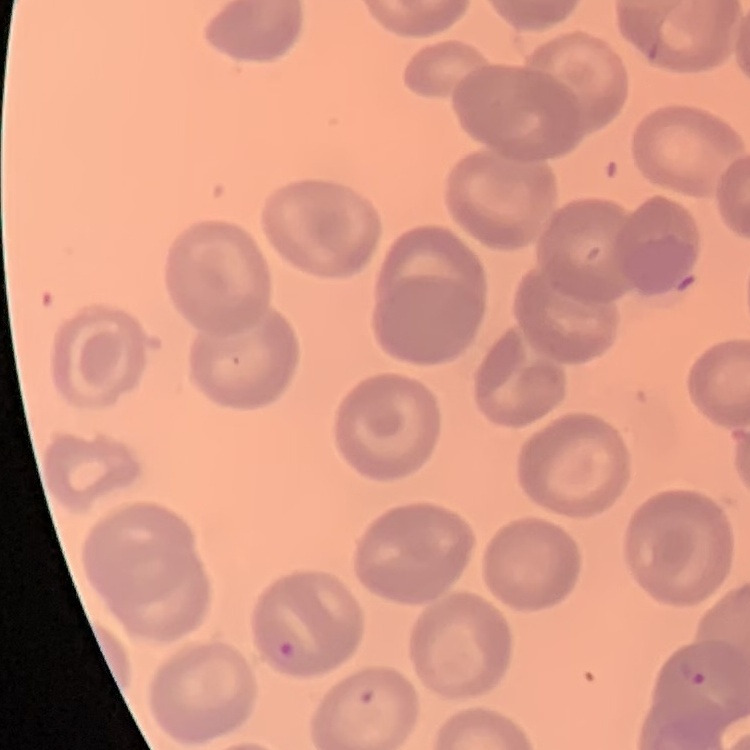
{
  "erythrocyte_morphology": "no rouleaux formation",
  "stain": "Field's or Giemsa",
  "preparation": "thin peripheral smear",
  "image_type": "one tile cut from a larger photomicrograph"
}